Report the malaria status of this cell.
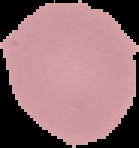

It is uninfected.

From a thin blood film. The area outside the segmented cell region is set to black. Image is 139×148 pixels.